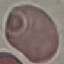

Summary:
  - Result: no malaria parasites seen
  - Preparation: thin blood film
  - Image type: automatically extracted cell patch, resized to 64 × 64 pixels
  - Stain: Giemsa
  - Capture: smartphone camera at the microscope eyepiece